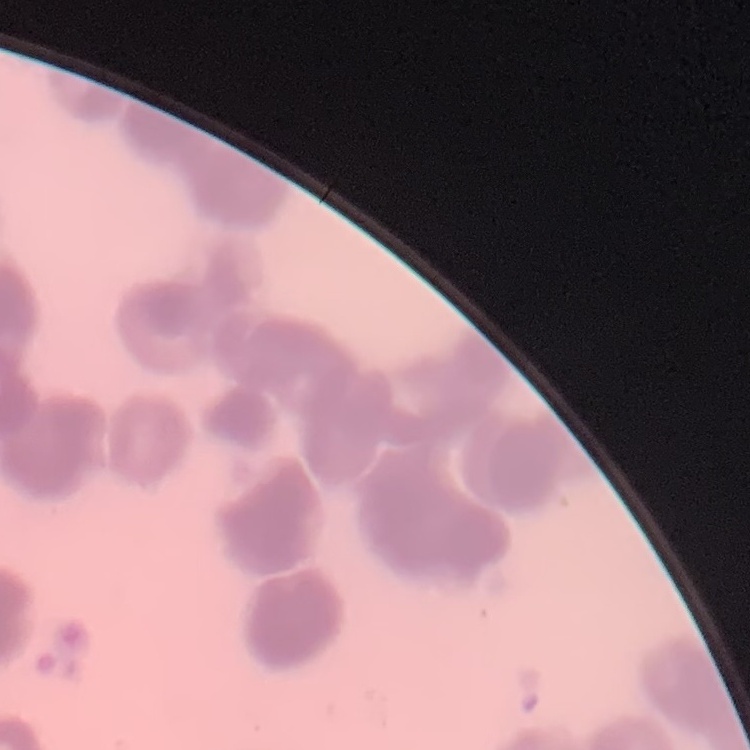
The red blood cells exhibit rouleaux formation. Stained with either Field's or Giemsa. Square crop of a larger photomicrograph. Thin blood smear.